Identify the cell.
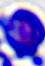

This is a leukocyte.

magnification: 400x
modality: photomicrograph